Locate every Plasmodium parasite.
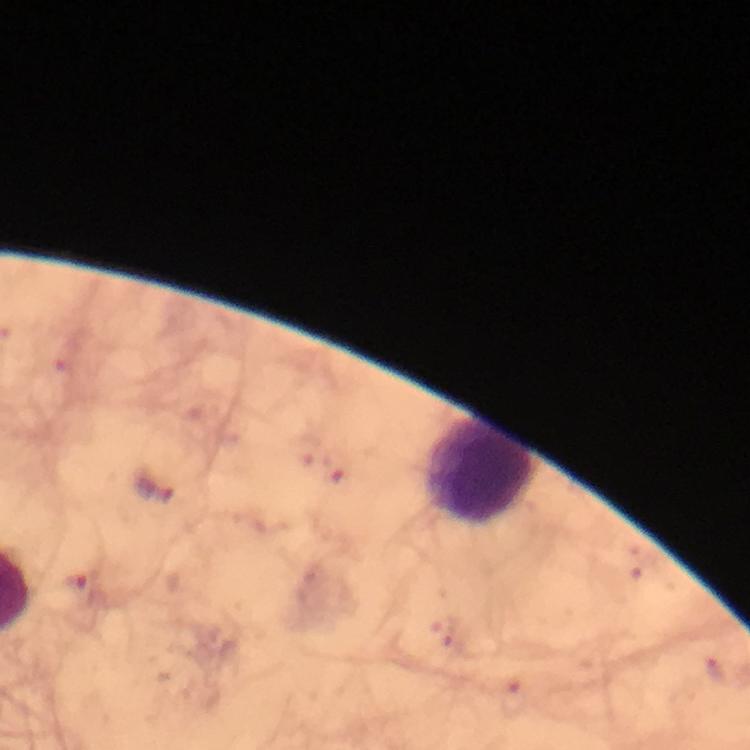
Approximate centers as (x, y) in pixels.
Plasmodium parasites: (155, 485), (82, 587).

Leukocyte locations: (480, 469). At 100x magnification. Thick blood smear. Giemsa stain. A crop from one field of view. Image is 750×750 pixels. Immersion oil applied. From a malaria diagnostic workup. Photographed with a smartphone mounted on the microscope.